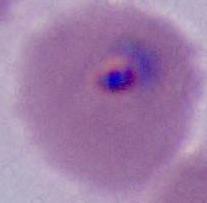 Captured at either 400x or 1000x magnification. A Plasmodium parasite is seen. Photomicrograph.